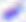
modality = photomicrograph
magnification = 400x
identification = Toxoplasma gondii